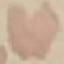

result = negative for malaria parasites
capture = smartphone through the microscope eyepiece
image type = cell patch, automatically extracted from a larger field of view and resized to 64 × 64 pixels
preparation = thin blood smear
stain = Giemsa